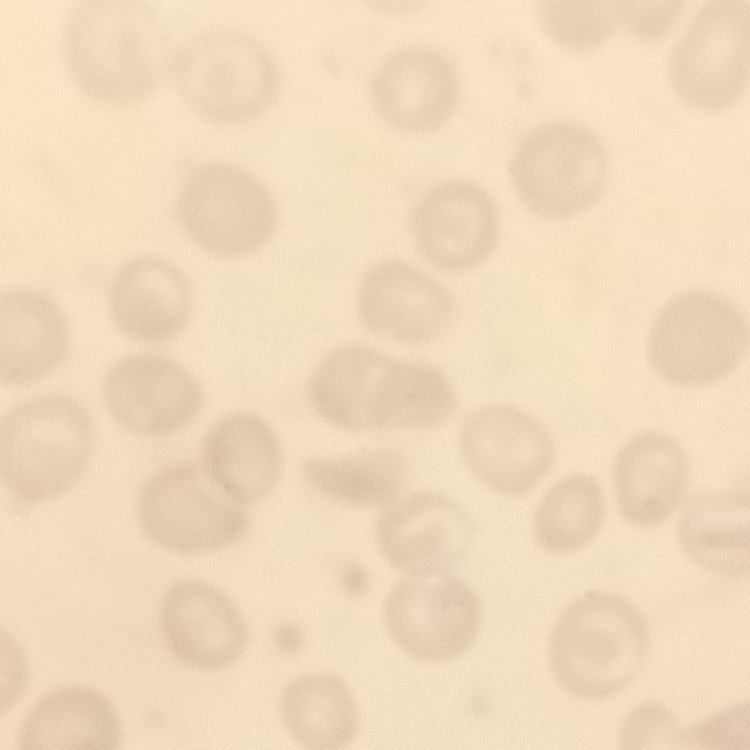

Summary:
  - Erythrocyte morphology: no rouleaux formation
  - Image type: one tile cut from a larger photomicrograph
  - Stain: Field's or Giemsa
  - Preparation: thin blood smear